Locate every blood parasite and identify its species.
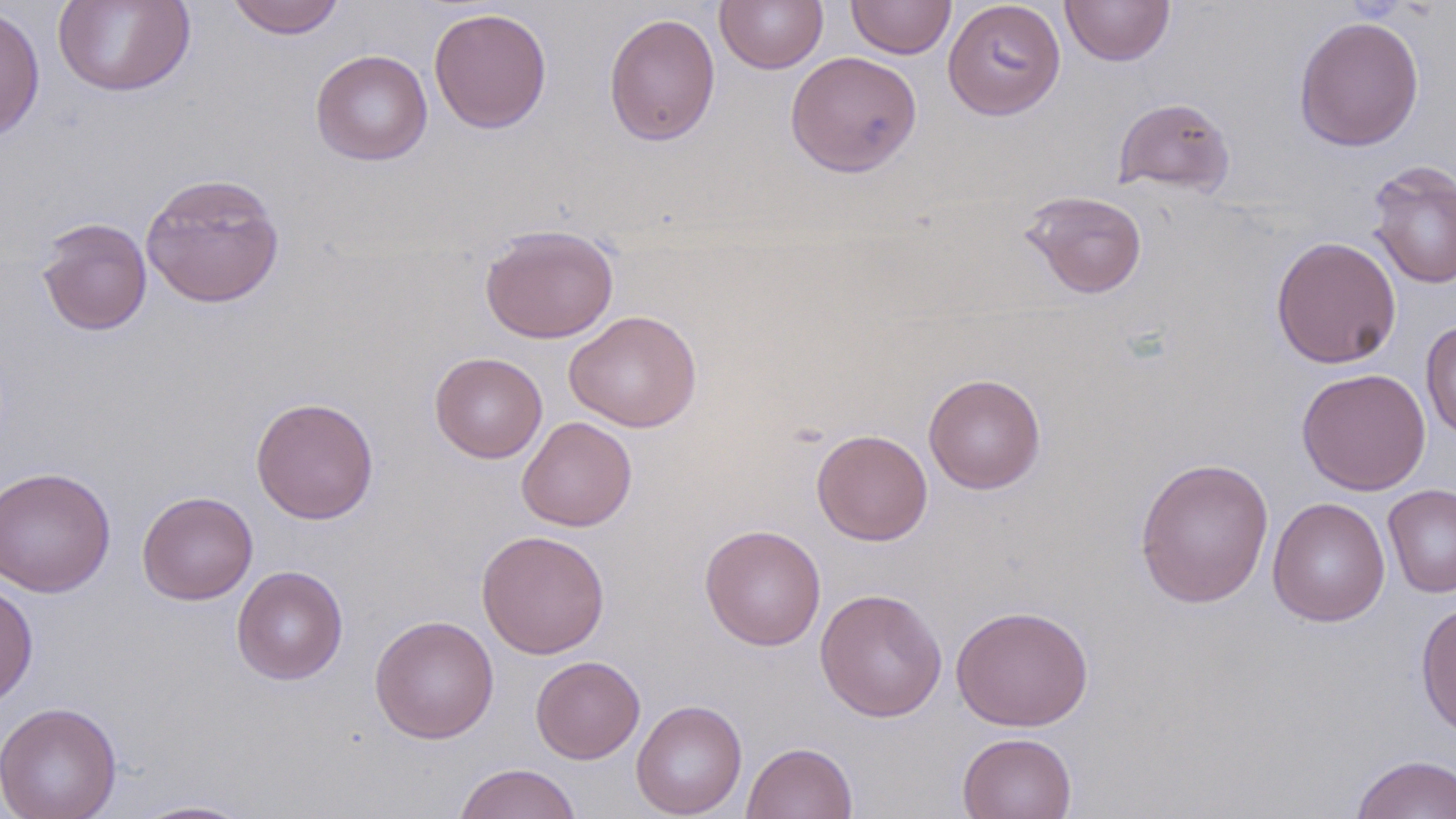
No blood parasites seen.

Summary:
  - Coordinate format: approximate bounding boxes as [x1, y1, x2, y2] in pixels
  - Uninfected red blood cell locations: [53, 0, 196, 98], [226, 0, 347, 40], [715, 0, 828, 74], [846, 0, 956, 59], [942, 0, 1066, 120], [1060, 0, 1175, 66], [0, 5, 45, 140], [429, 7, 552, 134], [604, 12, 721, 146], [1294, 15, 1424, 152], [310, 49, 432, 166], [785, 50, 922, 178], [1113, 97, 1235, 197], [1366, 160, 1456, 290], [140, 172, 285, 309], [1021, 190, 1148, 299], [36, 216, 153, 336], [479, 224, 619, 344], [1271, 235, 1401, 369], [564, 310, 702, 433], [1420, 319, 1456, 441], [429, 352, 547, 463], [1297, 367, 1431, 495], [923, 373, 1046, 494], [250, 396, 380, 525], [516, 416, 638, 532], [811, 428, 932, 545], [1134, 456, 1274, 609], [0, 466, 116, 597], [1383, 483, 1456, 598], [137, 490, 258, 605], [1267, 497, 1391, 626], [699, 524, 826, 651], [477, 529, 611, 658], [231, 565, 348, 685], [0, 579, 38, 710], [815, 588, 948, 722], [1415, 599, 1456, 740], [951, 605, 1093, 731], [369, 614, 499, 744], [530, 655, 645, 763], [631, 699, 747, 818], [0, 701, 122, 819], [957, 732, 1077, 819], [741, 741, 858, 819], [1350, 754, 1456, 819], [452, 763, 582, 819], [127, 799, 259, 818]
  - Slide-level diagnosis: no evidence of blood parasites
  - Preparation: thin blood smear
  - Field of view: one of a larger specimen
  - Image size: 1456×819 pixels
  - Stain: May-Grünwald-Giemsa
  - Modality: light microscopy
  - Magnification: 1000x